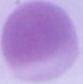
modality = micrograph
magnification = 1000x
identification = erythrocyte